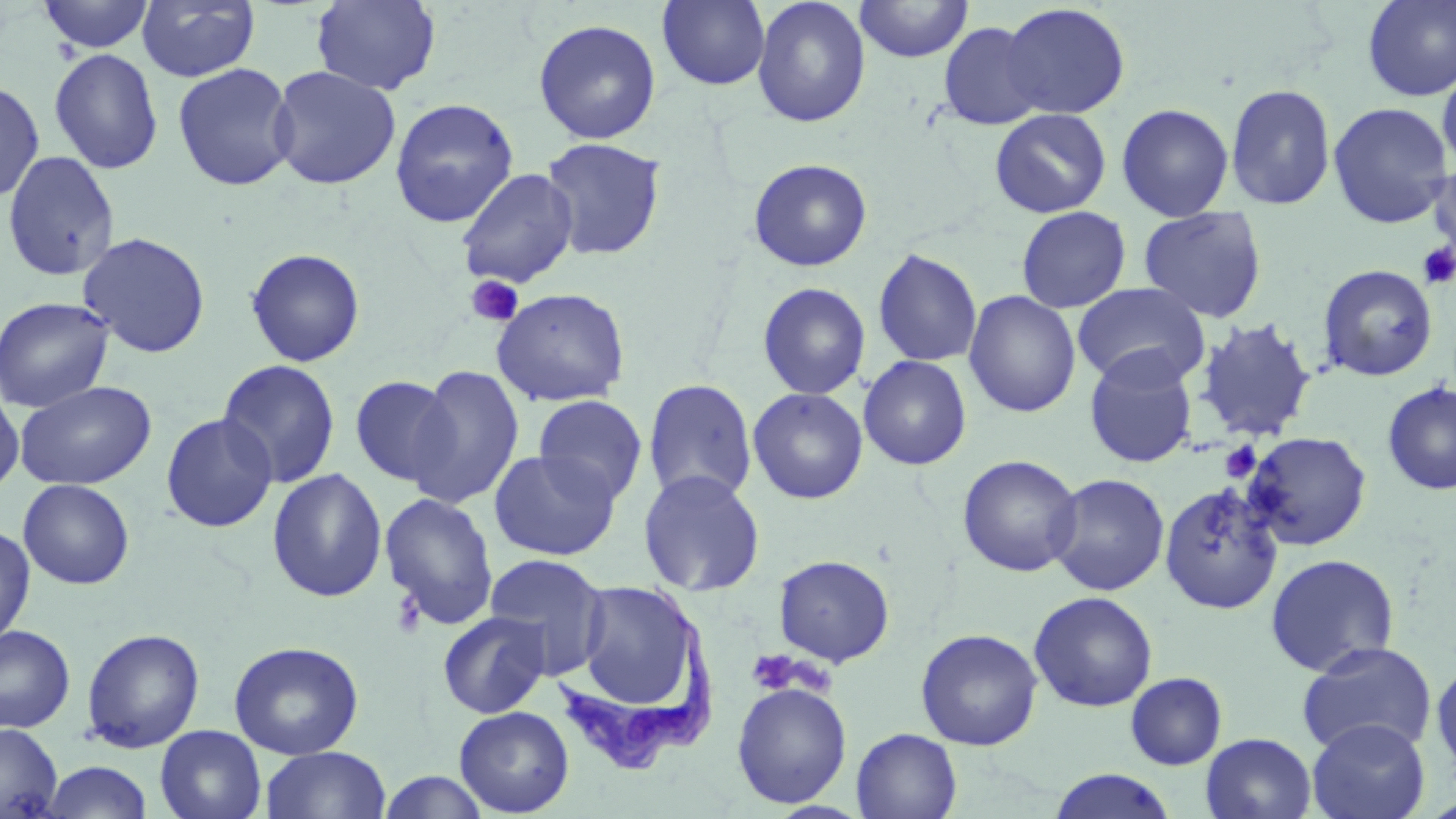
slide-level diagnosis = Trypanosoma brucei
stain = May-Grünwald-Giemsa
magnification = 1000x
uninfected red blood cell locations = approximate bounding boxes as [x1, y1, x2, y2] in pixels: [38, 0, 156, 53], [136, 0, 260, 82], [311, 0, 441, 95], [657, 0, 771, 90], [752, 0, 871, 127], [855, 0, 974, 62], [1360, 0, 1456, 102], [1000, 3, 1131, 120], [533, 19, 661, 144], [937, 21, 1046, 130], [49, 48, 164, 174], [1437, 57, 1456, 174], [172, 62, 297, 191], [267, 65, 402, 190], [0, 79, 44, 204], [1225, 83, 1336, 210], [389, 97, 519, 228], [1326, 102, 1453, 229], [1116, 103, 1235, 220], [989, 108, 1112, 218], [540, 137, 666, 261], [1, 149, 121, 282], [1430, 156, 1456, 262], [748, 158, 873, 272], [455, 168, 579, 289], [1015, 206, 1132, 313], [1138, 207, 1268, 323], [77, 231, 212, 358], [245, 247, 366, 367], [872, 248, 982, 367], [1317, 263, 1438, 382], [757, 282, 871, 400], [1073, 282, 1210, 390], [492, 287, 630, 407], [963, 290, 1081, 418], [0, 295, 115, 414], [1193, 318, 1318, 443], [1083, 350, 1199, 468], [858, 355, 972, 470], [217, 359, 341, 489], [408, 364, 525, 509], [349, 374, 458, 488], [642, 378, 758, 505], [15, 380, 157, 490], [1381, 382, 1456, 495], [0, 386, 25, 497], [748, 387, 868, 504], [532, 395, 648, 506], [160, 413, 278, 532], [1242, 431, 1372, 551], [488, 449, 621, 560], [957, 454, 1084, 577], [266, 468, 387, 603], [637, 469, 766, 597], [1046, 473, 1170, 596], [17, 478, 135, 589], [1158, 482, 1284, 615], [378, 491, 499, 631], [0, 524, 36, 649], [483, 553, 610, 678], [1264, 553, 1399, 676], [773, 554, 895, 667], [571, 577, 707, 723], [1028, 591, 1158, 712], [436, 611, 552, 719], [0, 625, 75, 734], [81, 627, 205, 753], [915, 627, 1043, 751], [228, 641, 364, 759], [1296, 641, 1437, 757], [1431, 657, 1456, 783], [1125, 672, 1227, 770], [731, 681, 852, 808], [454, 706, 575, 817], [1306, 717, 1430, 819], [0, 722, 62, 818], [155, 725, 267, 819], [851, 728, 962, 818], [1200, 732, 1317, 819], [260, 746, 391, 819], [38, 761, 155, 818], [1048, 769, 1179, 819], [377, 771, 491, 818]
platelet locations = approximate bounding boxes as [x1, y1, x2, y2] in pixels: [1418, 242, 1456, 289], [464, 274, 524, 329], [1220, 441, 1262, 482], [391, 588, 428, 640], [746, 650, 802, 695]
Trypanosoma brucei locations = approximate bounding boxes as [x1, y1, x2, y2] in pixels: [558, 580, 716, 776]
image size = 1456×819 pixels
preparation = thin blood film
modality = optical microscopy
field of view = single